Classify this cell by malaria status.
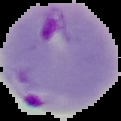

It is parasitized.

Summary:
  - Image type: segmented cell region with the area outside set to black
  - Preparation: thin blood film
  - Image size: 121×121 pixels